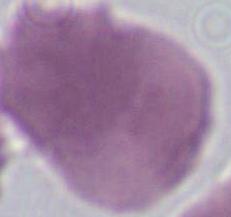
A red blood cell is shown. 1000x magnification. Micrograph.